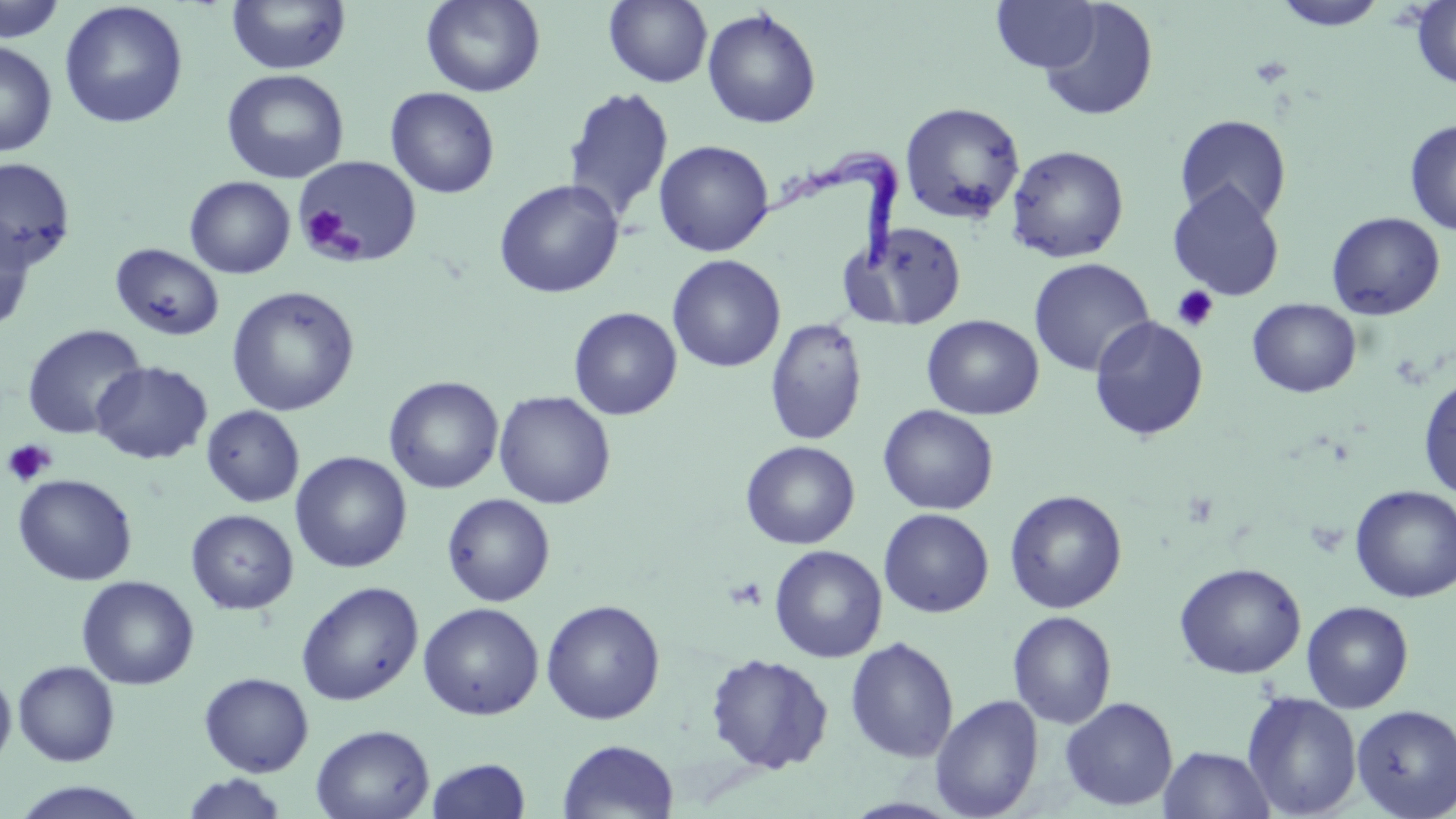

Approximate bounding boxes as named x1/y1/x2/y2 corners in pixels. Trypanosoma brucei locations: (x1=742, y1=147, x2=904, y2=276). Platelet locations: (x1=298, y1=206, x2=352, y2=257), (x1=1172, y1=285, x2=1219, y2=332), (x1=2, y1=439, x2=56, y2=486). Uninfected red blood cell locations: (x1=226, y1=0, x2=351, y2=76), (x1=420, y1=0, x2=546, y2=97), (x1=604, y1=0, x2=712, y2=87), (x1=991, y1=0, x2=1102, y2=72), (x1=1272, y1=0, x2=1389, y2=31), (x1=0, y1=1, x2=67, y2=43), (x1=59, y1=1, x2=188, y2=130), (x1=1410, y1=1, x2=1456, y2=90), (x1=1038, y1=2, x2=1159, y2=122), (x1=702, y1=8, x2=821, y2=129), (x1=0, y1=40, x2=57, y2=157), (x1=222, y1=68, x2=349, y2=184), (x1=563, y1=86, x2=674, y2=223), (x1=385, y1=87, x2=500, y2=199), (x1=900, y1=102, x2=1025, y2=225), (x1=1174, y1=114, x2=1292, y2=224), (x1=1404, y1=119, x2=1456, y2=236), (x1=653, y1=140, x2=775, y2=257), (x1=1006, y1=145, x2=1129, y2=263), (x1=295, y1=156, x2=422, y2=267), (x1=0, y1=157, x2=76, y2=270), (x1=185, y1=176, x2=296, y2=278), (x1=493, y1=179, x2=624, y2=299), (x1=1167, y1=181, x2=1285, y2=301), (x1=1326, y1=212, x2=1446, y2=321), (x1=0, y1=216, x2=36, y2=333), (x1=848, y1=221, x2=969, y2=330), (x1=111, y1=244, x2=224, y2=341), (x1=667, y1=254, x2=786, y2=373), (x1=1028, y1=257, x2=1155, y2=378), (x1=226, y1=286, x2=360, y2=416), (x1=1247, y1=298, x2=1361, y2=398), (x1=568, y1=307, x2=682, y2=420), (x1=922, y1=315, x2=1044, y2=420), (x1=1089, y1=316, x2=1209, y2=441), (x1=764, y1=317, x2=868, y2=446), (x1=22, y1=324, x2=147, y2=441), (x1=90, y1=361, x2=213, y2=465), (x1=1418, y1=375, x2=1456, y2=501), (x1=384, y1=376, x2=503, y2=494), (x1=494, y1=390, x2=616, y2=509), (x1=878, y1=404, x2=998, y2=515), (x1=201, y1=405, x2=304, y2=507), (x1=740, y1=441, x2=860, y2=549), (x1=290, y1=451, x2=412, y2=573), (x1=14, y1=473, x2=137, y2=586), (x1=1350, y1=485, x2=1455, y2=603), (x1=1004, y1=489, x2=1127, y2=613), (x1=441, y1=493, x2=556, y2=607), (x1=878, y1=508, x2=994, y2=618), (x1=186, y1=509, x2=298, y2=614), (x1=769, y1=544, x2=887, y2=663), (x1=1174, y1=562, x2=1306, y2=679), (x1=76, y1=575, x2=199, y2=690), (x1=296, y1=581, x2=423, y2=706), (x1=540, y1=599, x2=665, y2=724), (x1=1301, y1=600, x2=1414, y2=713), (x1=418, y1=602, x2=543, y2=720), (x1=1007, y1=611, x2=1117, y2=729), (x1=844, y1=636, x2=959, y2=763), (x1=704, y1=653, x2=833, y2=774), (x1=13, y1=660, x2=120, y2=766), (x1=0, y1=670, x2=16, y2=771), (x1=198, y1=672, x2=314, y2=777), (x1=1242, y1=691, x2=1362, y2=818), (x1=930, y1=695, x2=1043, y2=818), (x1=1060, y1=697, x2=1178, y2=812), (x1=1351, y1=704, x2=1456, y2=818), (x1=311, y1=724, x2=434, y2=819), (x1=557, y1=739, x2=679, y2=819), (x1=1158, y1=745, x2=1277, y2=818), (x1=426, y1=758, x2=532, y2=818), (x1=180, y1=773, x2=290, y2=819), (x1=11, y1=781, x2=150, y2=818). Slide-level diagnosis: Trypanosoma brucei. Image is 1456×819 pixels. Thin blood film. Optical microscopy. May-Grünwald-Giemsa-stained preparation. 1000x magnification. One field of a larger specimen.